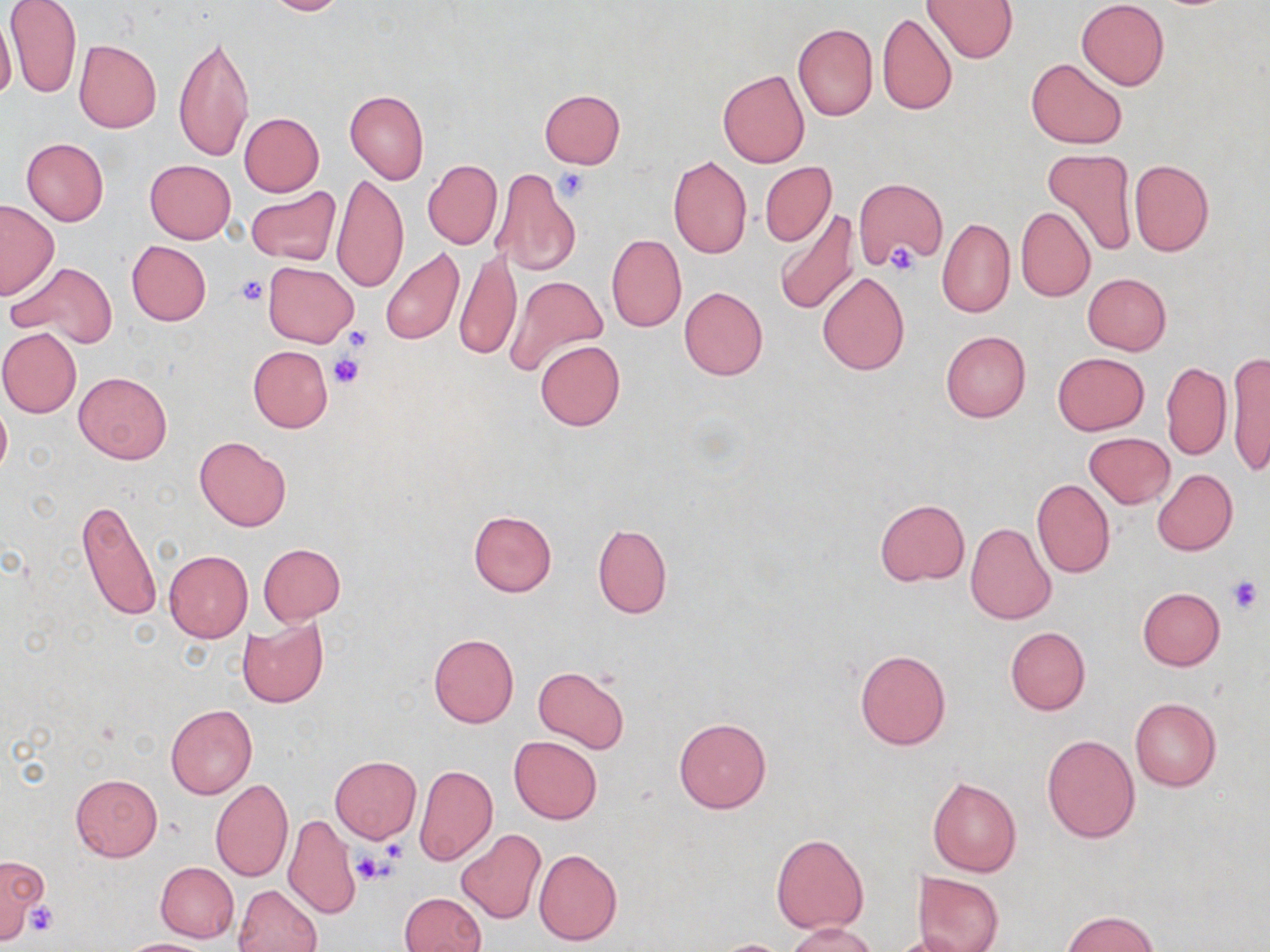 Approximate bounding boxes as [x1, y1, x2, y2] in pixels. Uninfected red blood cell locations: [261, 0, 349, 16], [923, 0, 1018, 63], [1076, 1, 1170, 90], [4, 2, 83, 101], [0, 13, 17, 106], [877, 13, 957, 115], [792, 22, 877, 121], [171, 28, 256, 166], [73, 39, 160, 133], [1026, 57, 1127, 149], [718, 69, 810, 168], [539, 89, 625, 168], [345, 90, 428, 184], [239, 113, 324, 196], [21, 139, 109, 225], [1039, 148, 1137, 257], [668, 155, 752, 259], [145, 159, 236, 243], [423, 160, 502, 249], [1129, 160, 1214, 256], [760, 162, 836, 246], [491, 168, 581, 278], [333, 173, 408, 294], [853, 177, 947, 270], [246, 186, 342, 266], [0, 199, 59, 298], [1016, 207, 1095, 301], [772, 210, 861, 315], [937, 217, 1015, 318], [606, 233, 686, 332], [126, 241, 211, 325], [379, 246, 464, 346], [455, 248, 522, 361], [7, 261, 118, 348], [264, 262, 357, 347], [817, 271, 910, 375], [1082, 273, 1171, 355], [503, 275, 608, 379], [679, 286, 768, 380], [0, 328, 82, 418], [941, 331, 1031, 422], [535, 340, 625, 431], [248, 345, 333, 431], [1052, 352, 1149, 435], [1226, 352, 1270, 479], [1161, 362, 1231, 460], [73, 371, 172, 463], [0, 401, 11, 481], [1085, 433, 1175, 508], [194, 435, 290, 531], [1153, 469, 1238, 555], [1031, 479, 1115, 579], [75, 498, 162, 624], [875, 499, 969, 585], [468, 509, 557, 596], [965, 522, 1056, 626], [592, 524, 671, 618], [258, 543, 346, 625], [164, 551, 253, 642], [1137, 587, 1225, 671], [236, 617, 327, 709], [1006, 626, 1090, 716], [428, 632, 518, 727], [855, 648, 950, 749], [533, 665, 629, 754], [1129, 698, 1221, 790], [165, 704, 257, 799], [675, 717, 771, 813], [509, 735, 602, 824], [1042, 735, 1139, 842], [330, 756, 421, 842], [415, 763, 498, 866], [69, 774, 163, 861], [927, 776, 1022, 878], [209, 778, 292, 881], [283, 814, 360, 919], [457, 830, 547, 925], [771, 834, 869, 933], [533, 849, 622, 946], [0, 858, 48, 941], [155, 861, 239, 942], [915, 872, 1004, 952], [233, 883, 321, 952], [399, 892, 486, 952], [1062, 910, 1160, 951], [785, 923, 882, 952], [891, 933, 972, 952], [120, 939, 215, 952], [711, 939, 794, 952]. Platelet locations: [556, 170, 590, 201], [886, 244, 918, 277], [234, 274, 269, 306], [343, 326, 373, 352], [327, 354, 364, 389], [1225, 576, 1264, 615], [381, 837, 408, 863], [352, 851, 391, 885], [25, 901, 57, 935]. Slide-level diagnosis: negative for blood parasites. Optical microscopy. May-Grünwald-Giemsa stain. Image is 1270×952 pixels. Thin blood smear. Single field of view. 1000x magnification.